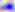
magnification = 400x
modality = micrograph
identification = Toxoplasma gondii